Outline each blood parasite and name the species.
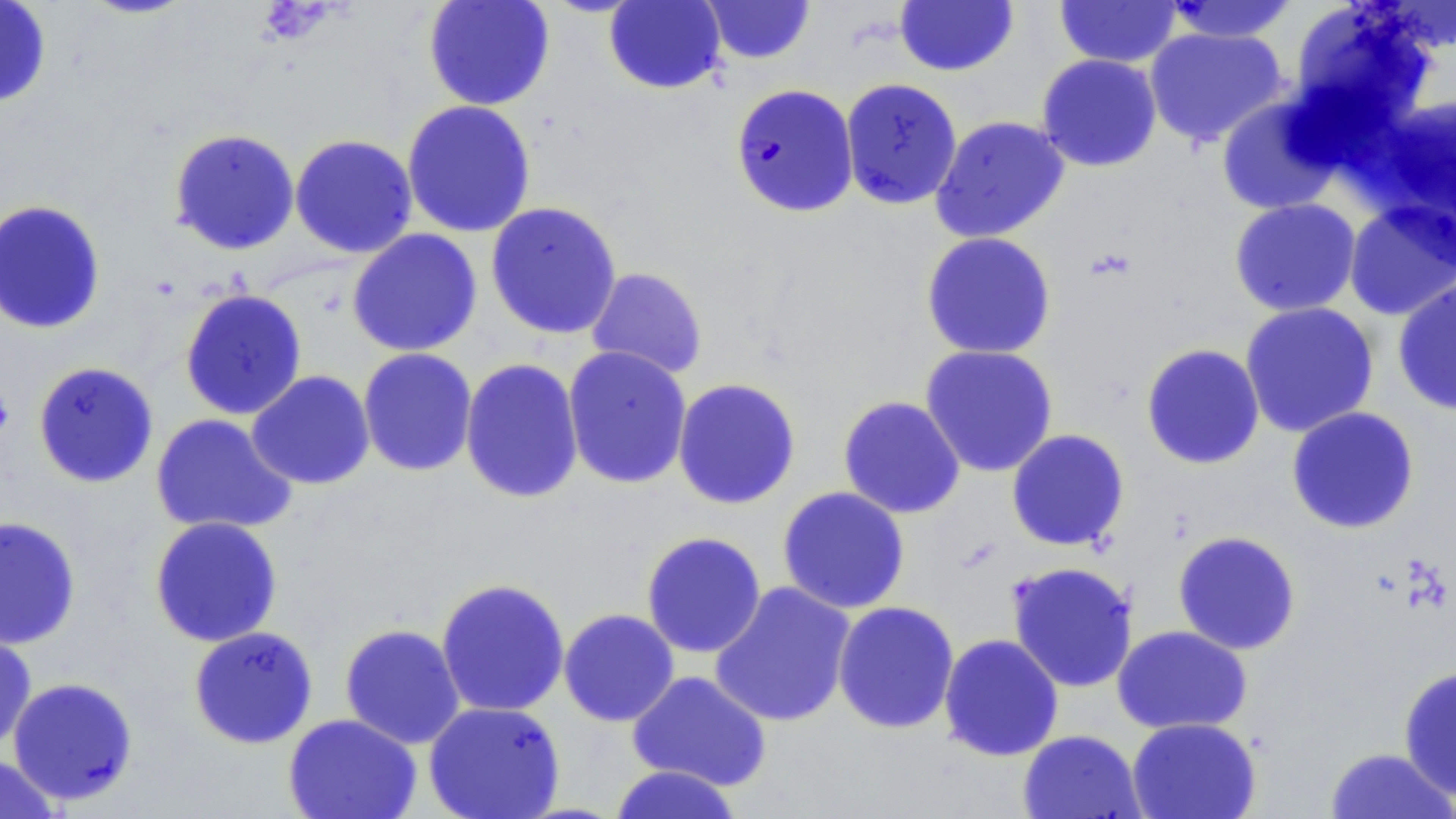

Approximate bounding boxes as (x1, y1, x2, y2) in pixels.
Plasmodium falciparum-infected red blood cells: (730, 83, 859, 217).
No Plasmodium ovale, Plasmodium malariae, Plasmodium vivax, Babesia divergens, or Trypanosoma brucei observed.

Summary:
  - Uninfected red blood cell locations: (0, 0, 52, 108), (78, 0, 198, 20), (422, 0, 556, 111), (604, 0, 727, 94), (894, 0, 1019, 77), (1363, 0, 1456, 53), (700, 1, 817, 65), (1053, 1, 1182, 68), (1162, 1, 1300, 43), (1288, 2, 1435, 131), (1144, 27, 1287, 148), (1036, 54, 1162, 172), (840, 78, 963, 211), (1215, 94, 1344, 216), (1369, 94, 1456, 232), (401, 100, 536, 238), (930, 115, 1071, 243), (168, 128, 300, 256), (290, 134, 418, 258), (1228, 197, 1361, 317), (0, 199, 106, 335), (1343, 199, 1456, 321), (485, 201, 623, 340), (347, 229, 483, 357), (920, 231, 1057, 359), (585, 267, 708, 380), (1392, 276, 1456, 416), (179, 289, 308, 421), (1239, 302, 1379, 437), (1140, 343, 1265, 470), (919, 344, 1059, 477), (562, 345, 692, 490), (357, 348, 477, 477), (460, 358, 584, 504), (32, 361, 159, 489), (246, 370, 375, 490), (672, 377, 801, 510), (837, 395, 966, 519), (1286, 406, 1421, 534), (150, 413, 298, 536), (1006, 429, 1130, 552), (776, 486, 911, 614), (0, 515, 82, 650), (149, 516, 283, 647), (1173, 530, 1302, 655), (641, 531, 767, 658), (1005, 561, 1139, 693), (435, 578, 570, 718), (709, 581, 856, 728), (832, 601, 960, 734), (558, 608, 680, 727), (339, 623, 465, 749), (1113, 625, 1252, 734), (188, 626, 319, 749), (0, 627, 37, 752), (938, 633, 1064, 761), (1398, 665, 1456, 801), (626, 670, 773, 791), (8, 676, 139, 804), (423, 701, 566, 818), (283, 713, 422, 819), (1126, 717, 1261, 819), (1017, 729, 1146, 819), (1323, 747, 1455, 819), (0, 755, 61, 819), (608, 764, 744, 819)
  - Slide-level diagnosis: Plasmodium falciparum
  - Field of view: one of a larger specimen
  - Stain: May-Grünwald-Giemsa
  - Image size: 1456×819 pixels
  - Modality: optical microscopy
  - Preparation: thin blood smear
  - Magnification: 1000x